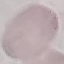
Malaria status: uninfected. Cell patch, automatically extracted from a larger field of view and resized to 64 × 64 pixels. Giemsa stain. Acquired by smartphone through the microscope eyepiece. Thin blood film.